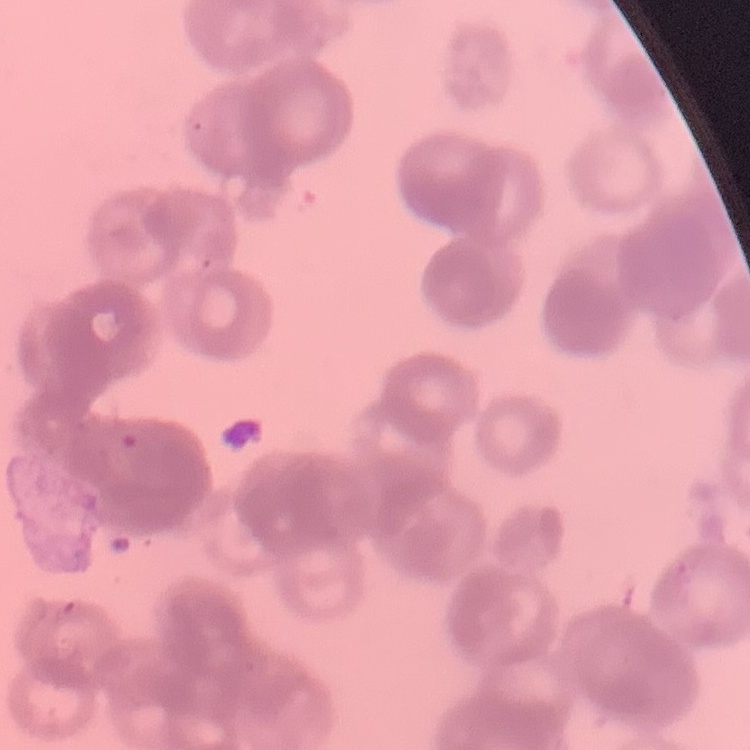
Summary:
  - Erythrocyte morphology: rouleaux formation
  - Image type: one tile cut from a larger photomicrograph
  - Stain: Field's or Giemsa
  - Preparation: thin blood smear